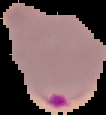

Summary:
  - Preparation: thin blood film
  - Image size: 106×115 pixels
  - Image type: segmented cell region with the area outside set to black
  - Result: Plasmodium parasites identified